Locate every Plasmodium parasite and every leukocyte.
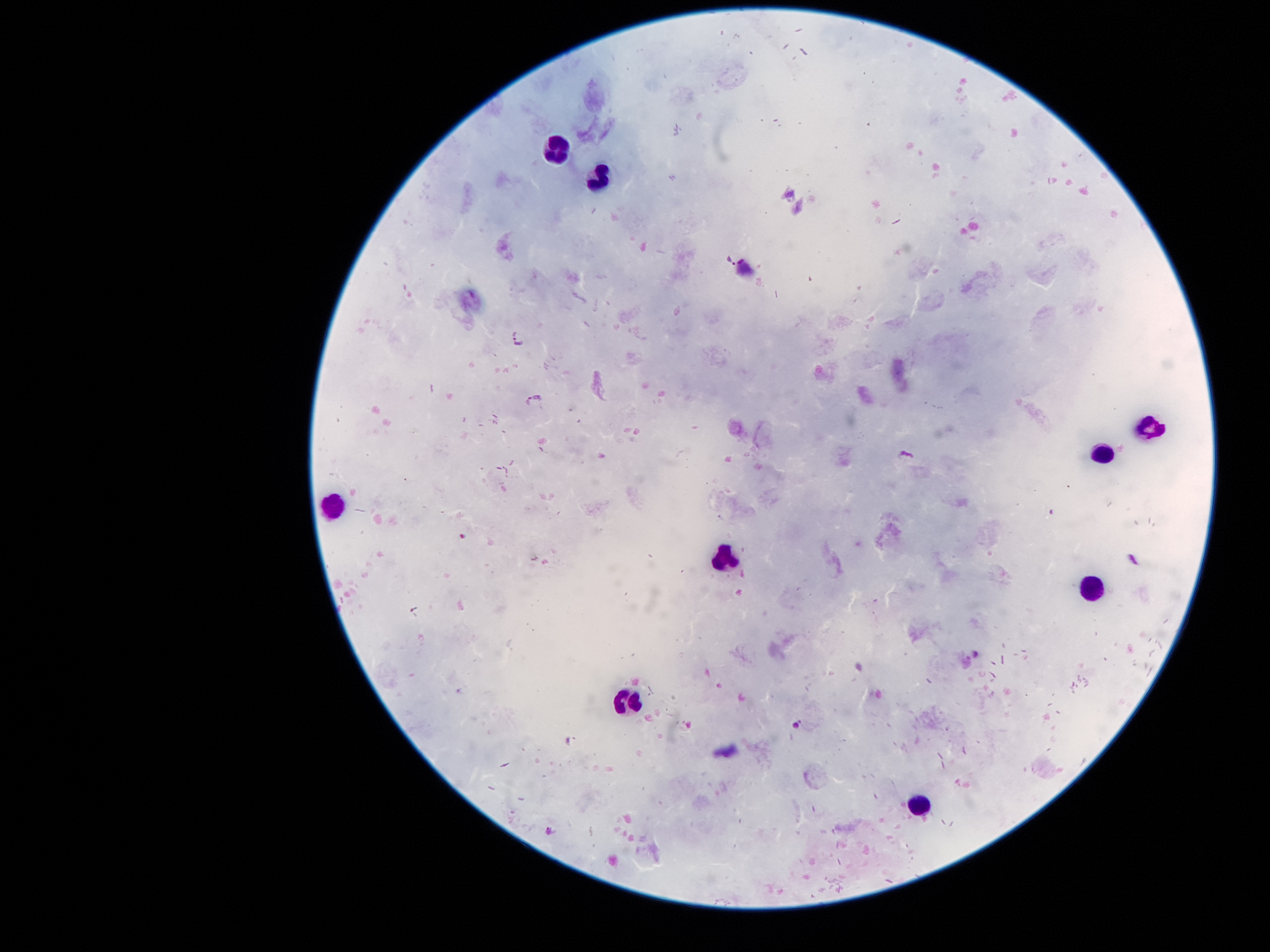

Approximate object centers, in pixels from the top-left corner.
Plasmodium parasites: (x=731, y=259), (x=522, y=336), (x=533, y=398), (x=906, y=455), (x=463, y=532), (x=797, y=722).
Leukocytes: (x=553, y=152), (x=598, y=177), (x=1150, y=426), (x=1105, y=452), (x=333, y=503), (x=721, y=561), (x=1089, y=588), (x=624, y=703), (x=918, y=804).

100x magnification. Giemsa-stained preparation. Single field of view. Smartphone photograph taken through the microscope eyepiece. Image is 1270×952 pixels. Thick peripheral-blood smear. Patient malaria status: infected with Plasmodium falciparum.